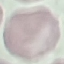
Summary:
  - Malaria status: uninfected
  - Capture: smartphone through the microscope eyepiece
  - Stain: Giemsa
  - Image type: automatically extracted cell patch, resized to 64 × 64 pixels
  - Preparation: thin blood smear